Classify this cell by malaria status.
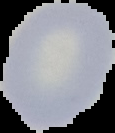
Uninfected.

Summary:
  - Image type: segmented cell region with the area outside set to black
  - Image size: 115×133 pixels
  - Preparation: thin blood smear